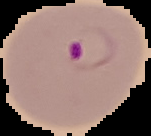

Summary:
  - Image size: 151×136 pixels
  - Image type: cell region segmented out of the field of view; surrounding area masked to black
  - Result: Plasmodium parasites detected
  - Preparation: thin blood film